Look for Plasmodium parasites.
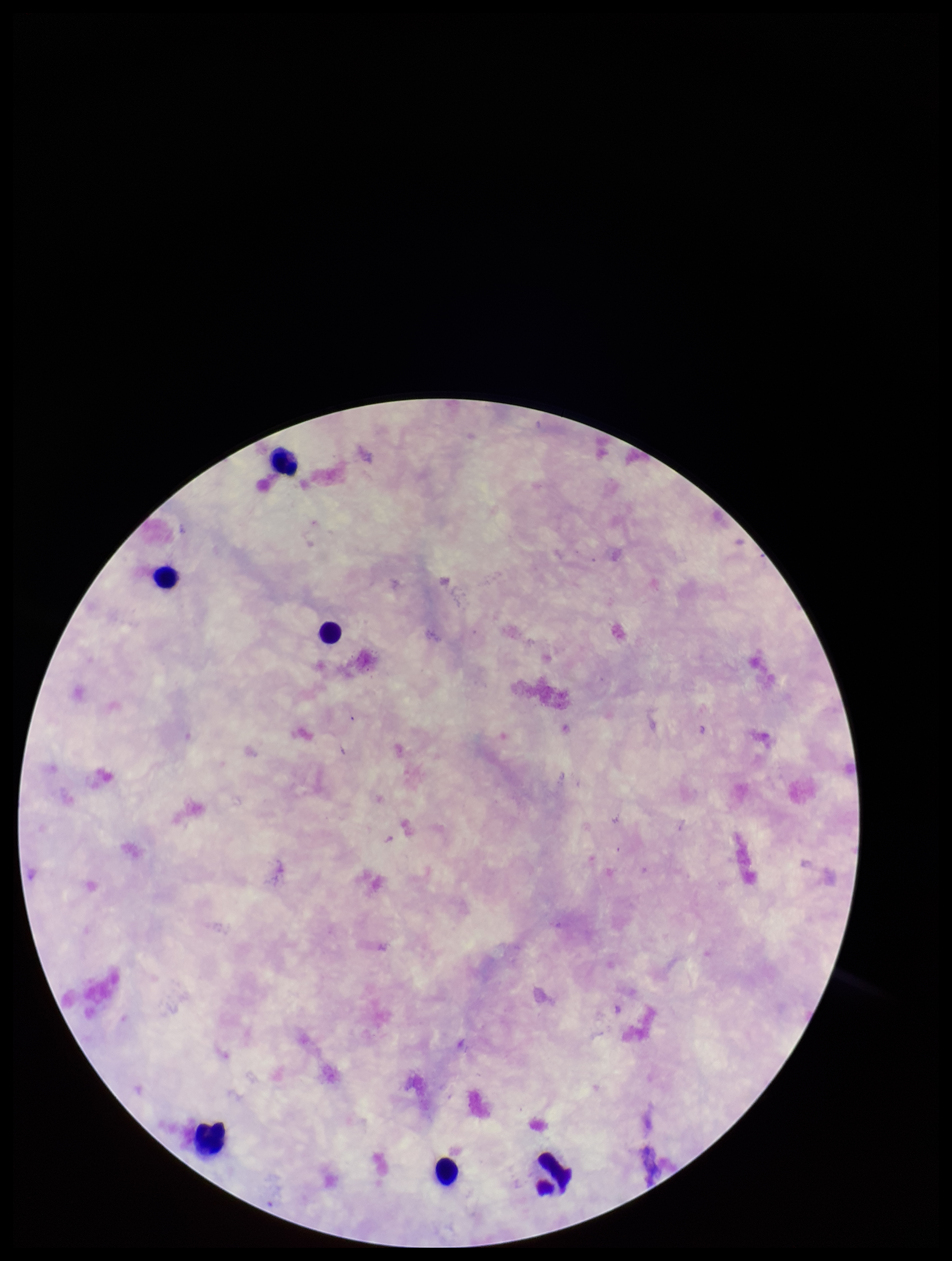

None detected.

Summary:
  - Preparation: thick smear
  - Image size: 952×1261 pixels
  - Parasite count: 0
  - Leukocyte count: 6
  - Capture: smartphone photograph through the microscope eyepiece
  - Patient malaria status: negative
  - Field of view: single
  - Stain: Giemsa